Locate every Plasmodium parasite by life-cycle stage, and every leukocyte.
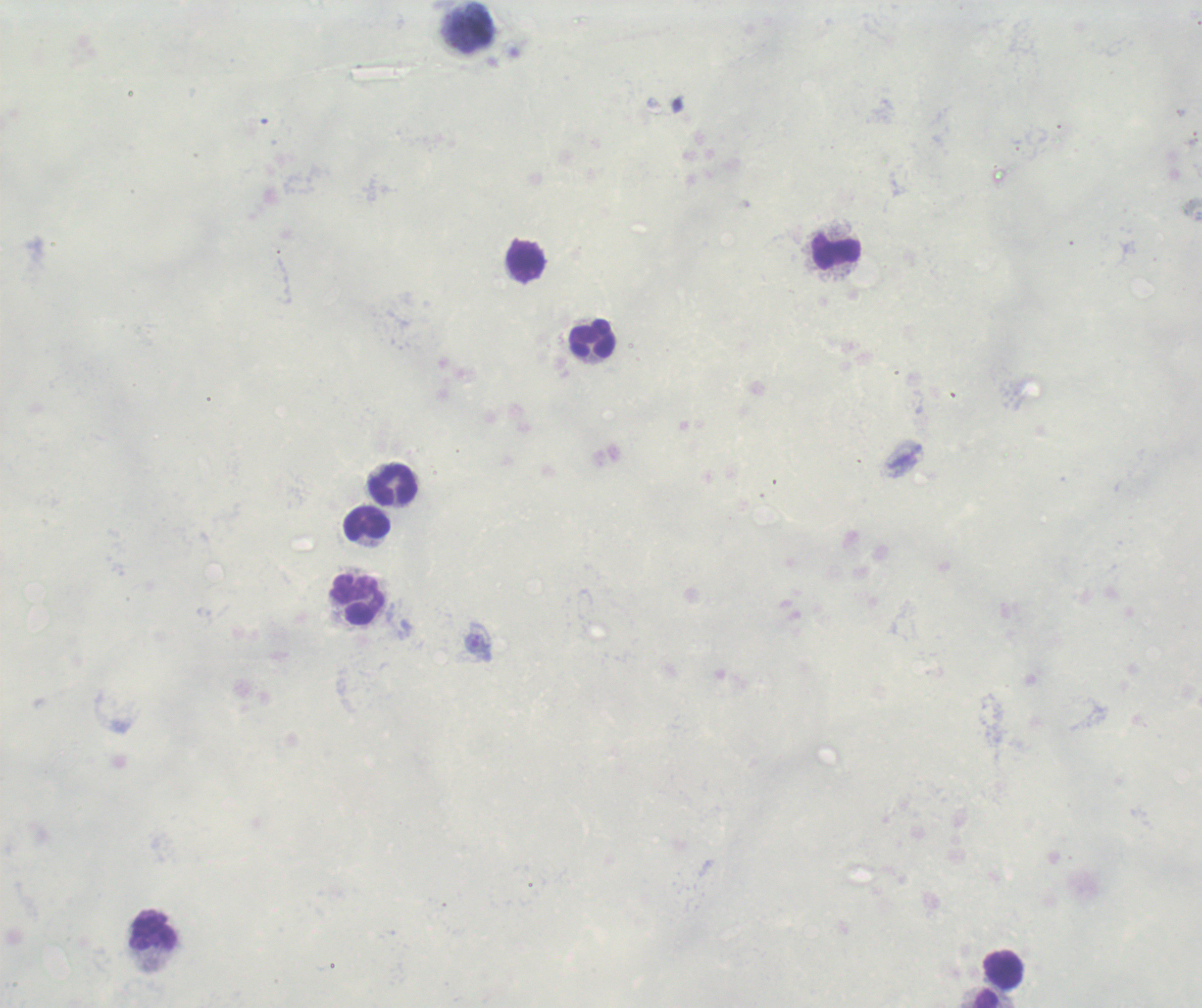

No Plasmodium parasites detected.
Approximate centers as (x, y) in pixels.
Leukocytes: (836, 252), (525, 261), (593, 339), (394, 486), (368, 523), (358, 600), (155, 930), (1004, 970), (987, 1000).

Summary:
  - Stain: Romanowsky
  - Preparation: thick blood smear
  - Magnification: 100x
  - Background quality: unsatisfactory
  - Field of view: single
  - Image size: 1202×1008 pixels
  - Context: previously used in an actual diagnosis